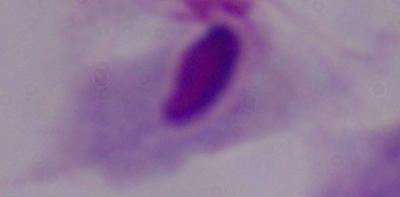
{
  "modality": "photomicrograph",
  "identification": "trichomonad",
  "magnification": "1000x"
}